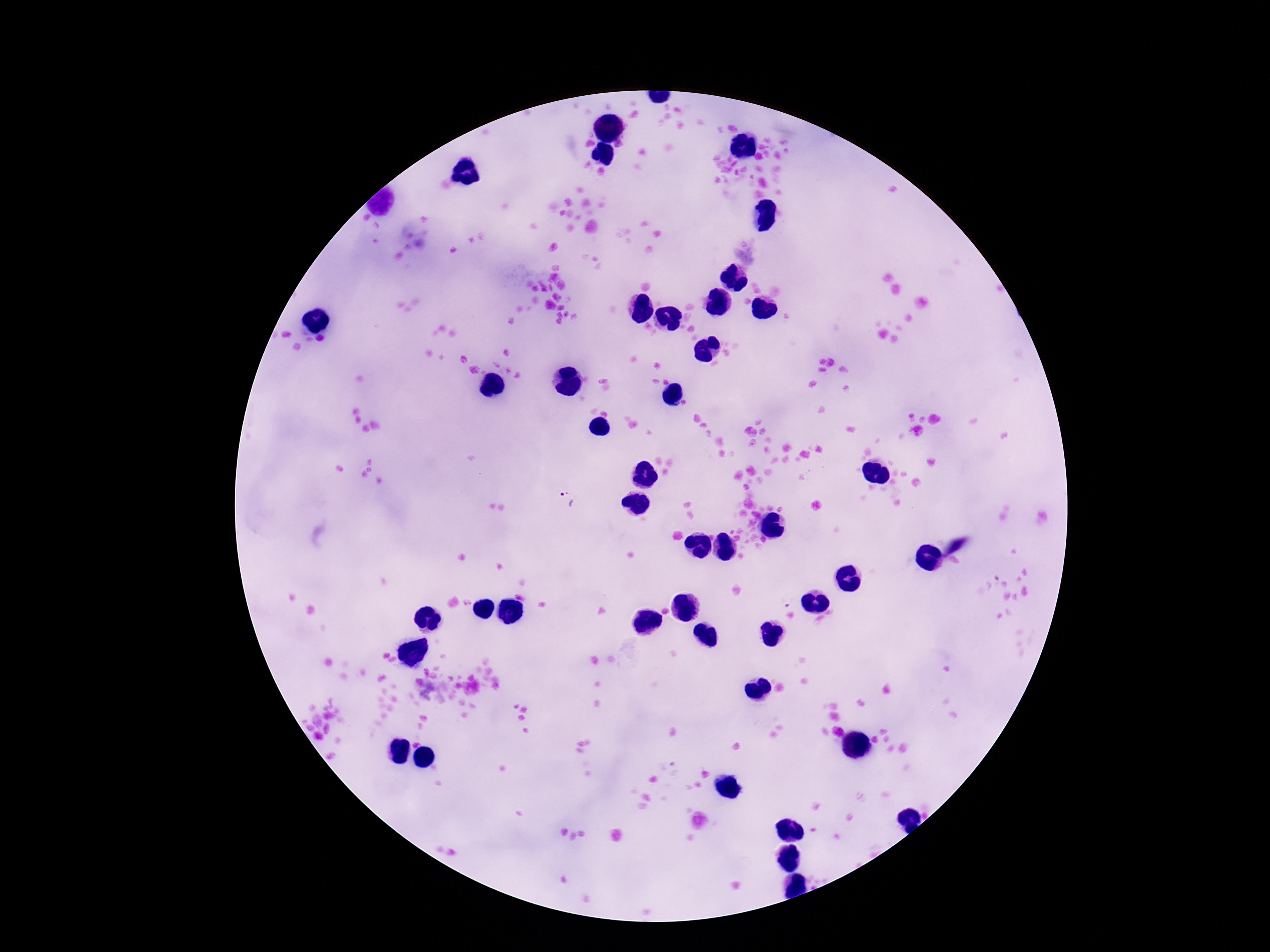
{
  "field_of_view": "one from this slide",
  "preparation": "thick blood smear",
  "capture": "smartphone camera through the microscope eyepiece",
  "image_size": "1270×952 pixels",
  "magnification": "100x",
  "patient_malaria_status": "positive",
  "stain": "Giemsa",
  "plasmodium_parasite_locations": "approximate centers as (x, y) in pixels: (566, 499), (786, 598)"
}